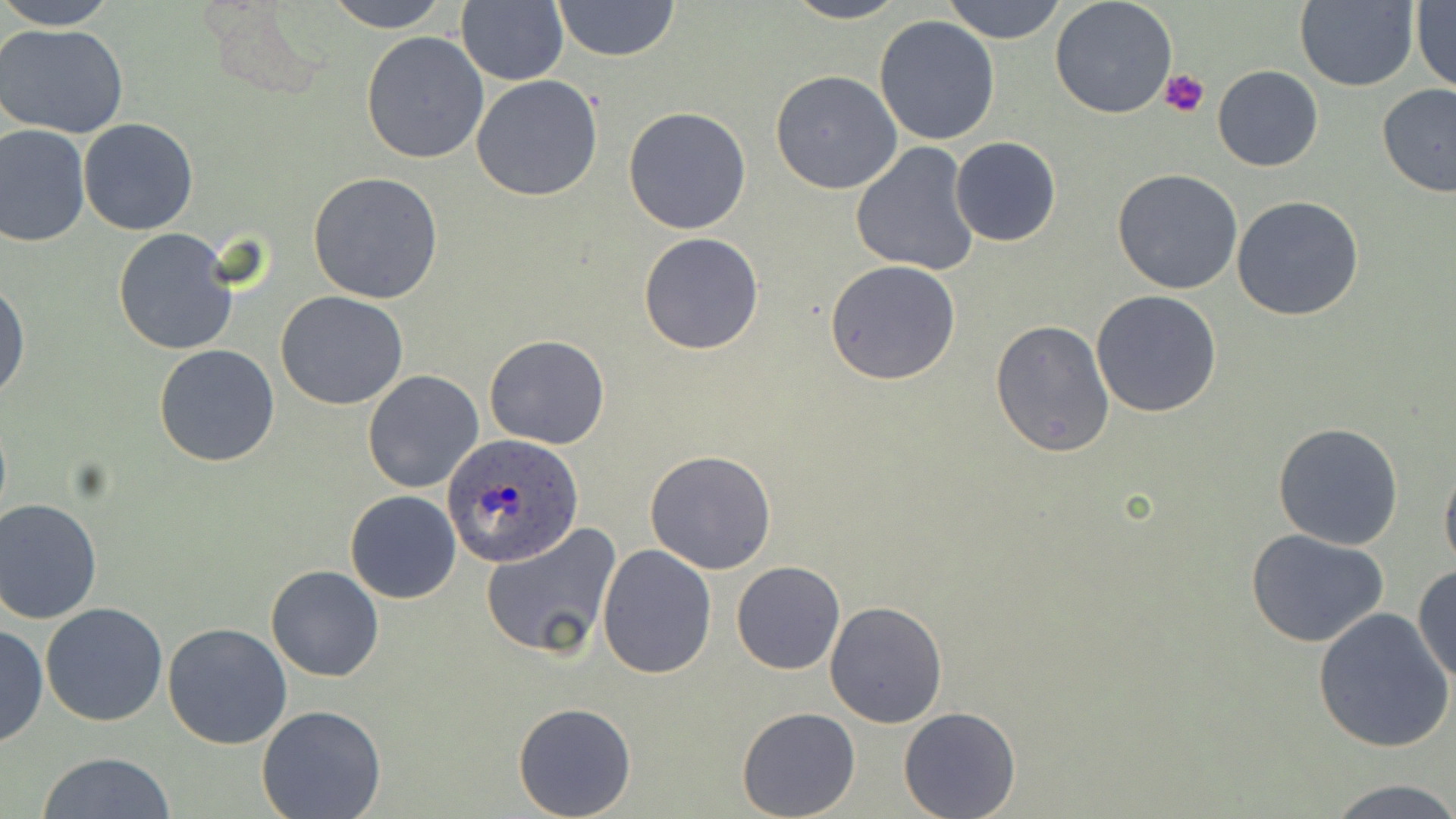

slide_level_diagnosis: Plasmodium ovale
preparation: thin blood smear
uninfected_red_blood_cell_locations: 'approximate bounding boxes as (x1,y1)-(x2,y2) corner pairs in pixels: (0,0)-(118,29), (321,0)-(453,32), (456,0)-(569,86), (551,0)-(679,61), (782,0)-(910,24), (942,0)-(1069,44), (1050,0)-(1179,120), (1294,1)-(1418,91), (1411,2)-(1456,93), (875,16)-(1000,145), (0,23)-(129,138), (360,32)-(489,163), (1212,65)-(1324,171), (770,70)-(902,194), (471,75)-(603,202), (1376,83)-(1456,197), (623,106)-(752,233), (79,119)-(199,235), (1,124)-(91,247), (949,137)-(1060,246), (850,141)-(982,277), (1113,169)-(1244,295), (308,173)-(443,304), (1232,195)-(1364,321), (112,228)-(240,356), (639,233)-(763,354), (825,260)-(963,385), (0,278)-(29,405), (1090,290)-(1223,416), (276,292)-(407,409), (989,318)-(1115,457), (484,334)-(609,450), (152,345)-(280,468), (362,370)-(484,494), (1271,422)-(1404,551), (646,450)-(778,574), (1440,458)-(1456,578), (345,491)-(461,604), (0,499)-(102,623), (479,522)-(622,660), (1245,527)-(1392,647), (596,544)-(717,679), (731,560)-(845,675), (1413,562)-(1456,686), (265,564)-(383,683), (823,601)-(948,727), (40,603)-(169,726), (1313,607)-(1454,753), (163,624)-(292,750), (0,625)-(48,750), (513,702)-(637,818), (256,704)-(387,819), (736,707)-(860,819), (899,707)-(1020,819), (35,752)-(176,819), (1322,776)-(1455,817)'
image_size: 1456×819 pixels
stain: May-Grünwald-Giemsa
magnification: 1000x
plasmodium_ovale_infected_red_blood_cell_locations: 'approximate bounding boxes as (x1,y1)-(x2,y2) corner pairs in pixels: (442,433)-(581,561)'
platelet_locations: 'approximate bounding boxes as (x1,y1)-(x2,y2) corner pairs in pixels: (1161,70)-(1209,117)'
field_of_view: one of a larger specimen
modality: optical microscopy